Classify this cell by malaria status.
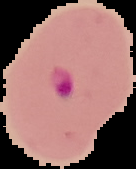

It is parasitized.

{
  "image_size": "136×169 pixels",
  "image_type": "segmented cell region on a black background",
  "preparation": "thin blood smear"
}